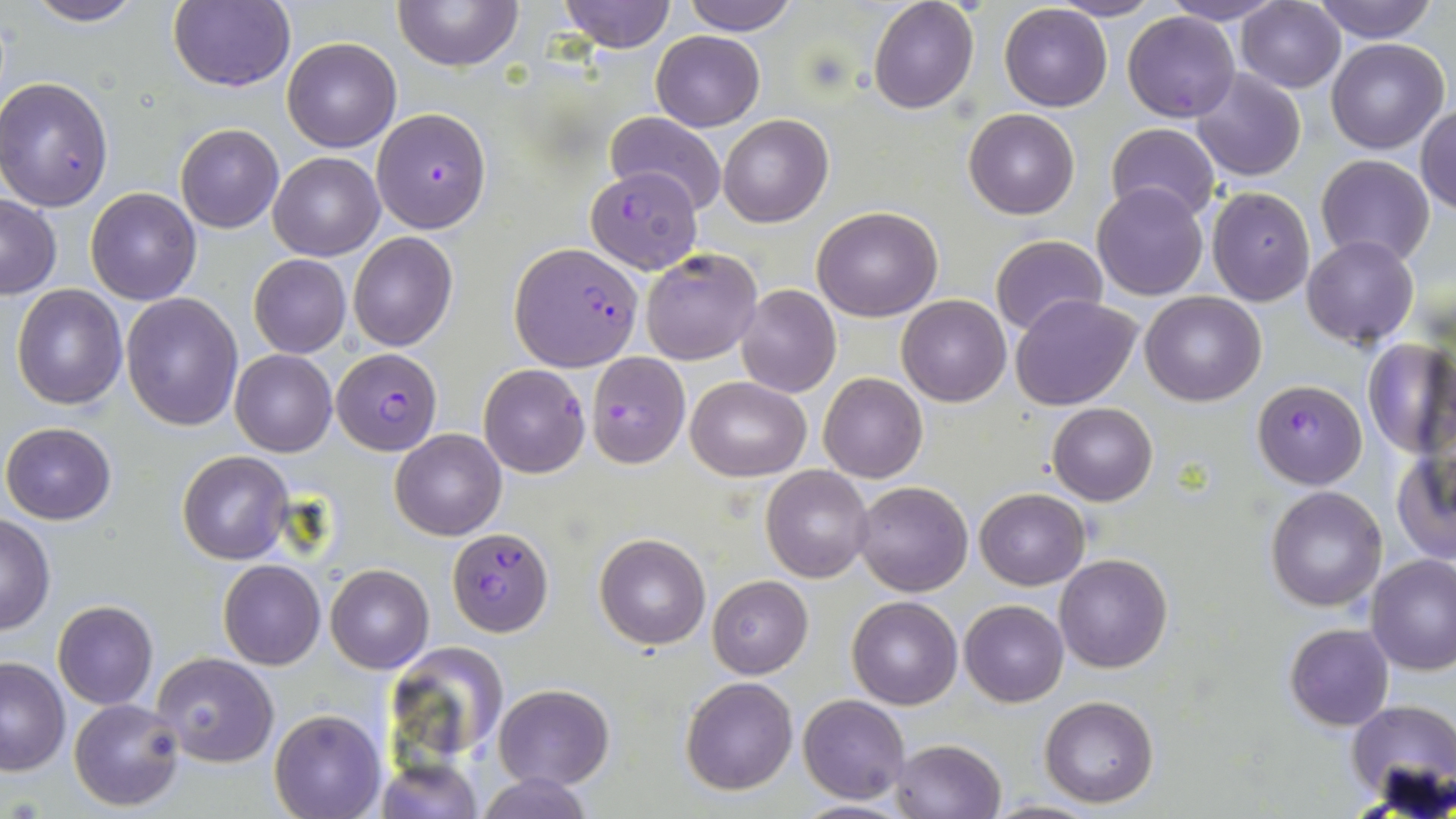

Summary:
  - Coordinate format: approximate bounding boxes as named x1/y1/x2/y2 corners in pixels
  - Uninfected red blood cell locations: (x1=20, y1=0, x2=145, y2=27), (x1=394, y1=0, x2=523, y2=71), (x1=560, y1=0, x2=676, y2=51), (x1=679, y1=0, x2=799, y2=36), (x1=868, y1=0, x2=979, y2=113), (x1=1049, y1=0, x2=1164, y2=21), (x1=1236, y1=0, x2=1345, y2=92), (x1=168, y1=1, x2=294, y2=93), (x1=1159, y1=1, x2=1286, y2=25), (x1=1309, y1=1, x2=1440, y2=43), (x1=999, y1=5, x2=1112, y2=112), (x1=1123, y1=11, x2=1240, y2=123), (x1=651, y1=31, x2=764, y2=131), (x1=282, y1=36, x2=401, y2=152), (x1=1326, y1=38, x2=1449, y2=155), (x1=1190, y1=68, x2=1307, y2=182), (x1=1, y1=77, x2=117, y2=212), (x1=1415, y1=106, x2=1456, y2=215), (x1=964, y1=109, x2=1079, y2=220), (x1=604, y1=111, x2=727, y2=215), (x1=717, y1=114, x2=833, y2=227), (x1=1106, y1=122, x2=1220, y2=222), (x1=176, y1=124, x2=284, y2=233), (x1=268, y1=151, x2=384, y2=260), (x1=1316, y1=155, x2=1436, y2=267), (x1=1092, y1=184, x2=1210, y2=300), (x1=1207, y1=186, x2=1315, y2=307), (x1=85, y1=187, x2=201, y2=305), (x1=1, y1=195, x2=60, y2=299), (x1=812, y1=205, x2=942, y2=321), (x1=348, y1=231, x2=459, y2=352), (x1=990, y1=235, x2=1107, y2=338), (x1=1302, y1=235, x2=1418, y2=349), (x1=641, y1=246, x2=762, y2=366), (x1=248, y1=253, x2=351, y2=358), (x1=11, y1=284, x2=127, y2=409), (x1=736, y1=285, x2=841, y2=397), (x1=121, y1=292, x2=244, y2=431), (x1=1011, y1=293, x2=1142, y2=411), (x1=1140, y1=293, x2=1266, y2=406), (x1=896, y1=295, x2=1012, y2=406), (x1=1361, y1=338, x2=1456, y2=458), (x1=229, y1=350, x2=338, y2=457), (x1=478, y1=363, x2=591, y2=479), (x1=819, y1=372, x2=927, y2=484), (x1=687, y1=376, x2=811, y2=481), (x1=1047, y1=403, x2=1157, y2=505), (x1=1, y1=422, x2=118, y2=524), (x1=390, y1=429, x2=506, y2=540), (x1=1391, y1=446, x2=1456, y2=566), (x1=178, y1=450, x2=294, y2=564), (x1=760, y1=465, x2=875, y2=582), (x1=852, y1=481, x2=973, y2=596), (x1=1265, y1=486, x2=1387, y2=612), (x1=973, y1=488, x2=1090, y2=590), (x1=0, y1=514, x2=55, y2=633), (x1=593, y1=533, x2=711, y2=650), (x1=1054, y1=553, x2=1173, y2=674), (x1=1365, y1=555, x2=1456, y2=675), (x1=218, y1=558, x2=327, y2=669), (x1=326, y1=565, x2=433, y2=673), (x1=707, y1=575, x2=813, y2=677), (x1=848, y1=595, x2=962, y2=708), (x1=960, y1=600, x2=1069, y2=707), (x1=52, y1=601, x2=158, y2=709), (x1=1285, y1=624, x2=1394, y2=730), (x1=385, y1=643, x2=509, y2=768), (x1=150, y1=653, x2=279, y2=768), (x1=0, y1=658, x2=71, y2=775), (x1=680, y1=676, x2=799, y2=794), (x1=493, y1=683, x2=616, y2=789), (x1=798, y1=695, x2=909, y2=803), (x1=1039, y1=696, x2=1159, y2=806), (x1=69, y1=698, x2=185, y2=812), (x1=1346, y1=700, x2=1456, y2=808), (x1=270, y1=710, x2=385, y2=818), (x1=890, y1=738, x2=1006, y2=819), (x1=372, y1=758, x2=481, y2=817), (x1=477, y1=773, x2=591, y2=818), (x1=986, y1=798, x2=1101, y2=818), (x1=786, y1=800, x2=917, y2=817)
  - Plasmodium falciparum-infected red blood cell locations: (x1=371, y1=108, x2=491, y2=233), (x1=587, y1=167, x2=700, y2=273), (x1=510, y1=243, x2=642, y2=370), (x1=332, y1=348, x2=443, y2=455), (x1=587, y1=352, x2=690, y2=469), (x1=1251, y1=379, x2=1367, y2=488), (x1=447, y1=528, x2=552, y2=636)
  - Slide-level diagnosis: Plasmodium falciparum
  - Magnification: 1000x
  - Preparation: thin blood film
  - Image size: 1456×819 pixels
  - Field of view: one of a larger specimen
  - Stain: May-Grünwald-Giemsa
  - Modality: optical microscopy